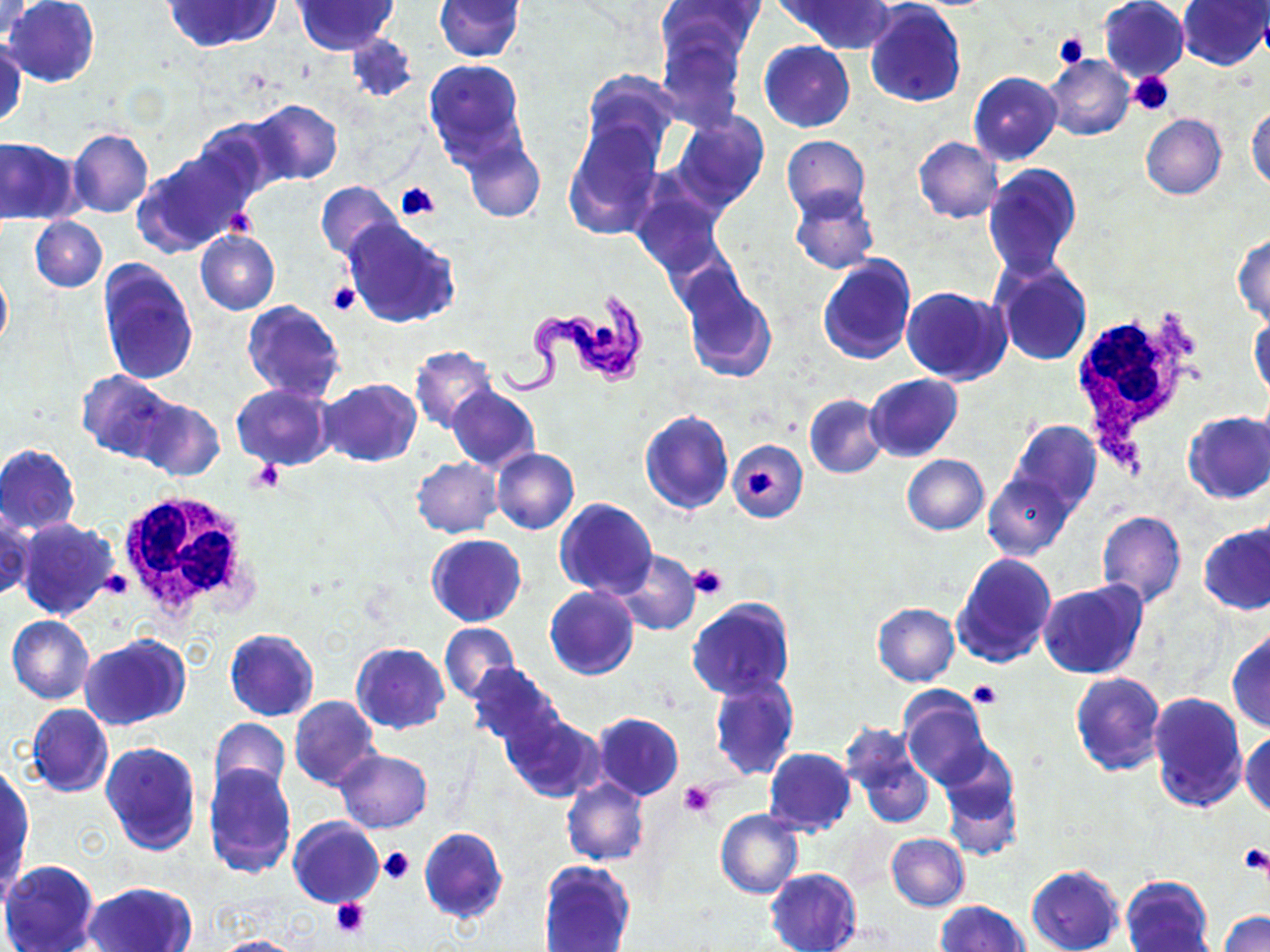

Summary:
  - Coordinate format: approximate bounding boxes as named x1/y1/x2/y2 corners in pixels
  - White blood cell locations: (x1=1066, y1=296, x2=1197, y2=477), (x1=115, y1=489, x2=262, y2=627)
  - Platelet locations: (x1=1051, y1=31, x2=1089, y2=69), (x1=1129, y1=71, x2=1176, y2=115), (x1=395, y1=183, x2=440, y2=222), (x1=224, y1=209, x2=258, y2=240), (x1=327, y1=281, x2=361, y2=317), (x1=248, y1=460, x2=286, y2=494), (x1=746, y1=469, x2=779, y2=497), (x1=689, y1=563, x2=729, y2=599), (x1=102, y1=567, x2=132, y2=598), (x1=968, y1=680, x2=1002, y2=707), (x1=679, y1=781, x2=717, y2=818), (x1=1240, y1=842, x2=1270, y2=877), (x1=379, y1=847, x2=414, y2=885), (x1=331, y1=897, x2=371, y2=939)
  - Uninfected red blood cell locations: (x1=0, y1=0, x2=35, y2=41), (x1=5, y1=0, x2=98, y2=87), (x1=165, y1=0, x2=278, y2=51), (x1=433, y1=0, x2=523, y2=60), (x1=789, y1=0, x2=896, y2=52), (x1=1098, y1=0, x2=1190, y2=82), (x1=1178, y1=0, x2=1269, y2=70), (x1=293, y1=1, x2=398, y2=54), (x1=656, y1=1, x2=758, y2=72), (x1=864, y1=1, x2=966, y2=107), (x1=345, y1=33, x2=417, y2=101), (x1=656, y1=36, x2=746, y2=133), (x1=1, y1=39, x2=25, y2=131), (x1=760, y1=41, x2=854, y2=131), (x1=1044, y1=56, x2=1135, y2=141), (x1=424, y1=58, x2=530, y2=172), (x1=580, y1=69, x2=681, y2=168), (x1=968, y1=71, x2=1062, y2=166), (x1=245, y1=99, x2=343, y2=187), (x1=1247, y1=107, x2=1270, y2=191), (x1=668, y1=111, x2=769, y2=211), (x1=1140, y1=114, x2=1227, y2=199), (x1=191, y1=119, x2=283, y2=206), (x1=562, y1=120, x2=664, y2=239), (x1=68, y1=128, x2=153, y2=218), (x1=781, y1=134, x2=870, y2=221), (x1=0, y1=137, x2=80, y2=225), (x1=462, y1=137, x2=545, y2=223), (x1=913, y1=137, x2=1003, y2=223), (x1=134, y1=149, x2=250, y2=257), (x1=984, y1=164, x2=1082, y2=279), (x1=628, y1=178, x2=727, y2=278), (x1=315, y1=181, x2=402, y2=262), (x1=789, y1=187, x2=879, y2=275), (x1=30, y1=216, x2=106, y2=292), (x1=342, y1=219, x2=461, y2=328), (x1=195, y1=230, x2=280, y2=315), (x1=1233, y1=233, x2=1270, y2=325), (x1=817, y1=254, x2=917, y2=365), (x1=992, y1=259, x2=1092, y2=365), (x1=97, y1=260, x2=199, y2=385), (x1=0, y1=266, x2=11, y2=353), (x1=680, y1=277, x2=778, y2=384), (x1=902, y1=287, x2=1010, y2=385), (x1=242, y1=300, x2=346, y2=402), (x1=1250, y1=312, x2=1269, y2=401), (x1=409, y1=345, x2=499, y2=434), (x1=77, y1=371, x2=177, y2=461), (x1=866, y1=374, x2=963, y2=462), (x1=319, y1=378, x2=421, y2=466), (x1=233, y1=384, x2=334, y2=470), (x1=447, y1=385, x2=539, y2=473), (x1=804, y1=394, x2=887, y2=479), (x1=135, y1=396, x2=223, y2=481), (x1=639, y1=411, x2=733, y2=515), (x1=1183, y1=411, x2=1270, y2=503), (x1=1007, y1=419, x2=1101, y2=515), (x1=727, y1=439, x2=808, y2=525), (x1=0, y1=444, x2=81, y2=534), (x1=492, y1=447, x2=579, y2=534), (x1=902, y1=454, x2=989, y2=534), (x1=411, y1=457, x2=502, y2=537), (x1=983, y1=473, x2=1076, y2=558), (x1=554, y1=499, x2=658, y2=600), (x1=1, y1=510, x2=33, y2=602), (x1=1095, y1=510, x2=1186, y2=608), (x1=14, y1=518, x2=120, y2=621), (x1=1200, y1=522, x2=1269, y2=614), (x1=426, y1=535, x2=525, y2=627), (x1=611, y1=550, x2=700, y2=636), (x1=952, y1=552, x2=1057, y2=669), (x1=1037, y1=581, x2=1146, y2=680), (x1=544, y1=586, x2=637, y2=680), (x1=686, y1=598, x2=795, y2=698), (x1=871, y1=603, x2=960, y2=686), (x1=7, y1=615, x2=95, y2=703), (x1=440, y1=623, x2=518, y2=704), (x1=225, y1=629, x2=319, y2=721), (x1=1227, y1=629, x2=1270, y2=732), (x1=81, y1=635, x2=189, y2=730), (x1=351, y1=642, x2=450, y2=734), (x1=465, y1=662, x2=565, y2=751), (x1=1070, y1=671, x2=1166, y2=775), (x1=709, y1=675, x2=799, y2=782), (x1=899, y1=686, x2=993, y2=790), (x1=1147, y1=691, x2=1248, y2=812), (x1=289, y1=694, x2=380, y2=790), (x1=27, y1=704, x2=113, y2=797), (x1=593, y1=713, x2=684, y2=800), (x1=503, y1=714, x2=604, y2=802), (x1=209, y1=718, x2=292, y2=803), (x1=843, y1=727, x2=935, y2=830), (x1=1241, y1=728, x2=1270, y2=818), (x1=100, y1=741, x2=202, y2=854), (x1=938, y1=744, x2=1023, y2=860), (x1=763, y1=748, x2=857, y2=836), (x1=336, y1=749, x2=432, y2=833), (x1=202, y1=763, x2=297, y2=879), (x1=1, y1=766, x2=32, y2=875), (x1=562, y1=778, x2=649, y2=866), (x1=716, y1=808, x2=803, y2=898), (x1=288, y1=817, x2=384, y2=907), (x1=419, y1=827, x2=508, y2=925), (x1=886, y1=832, x2=969, y2=912), (x1=1, y1=859, x2=99, y2=952), (x1=539, y1=859, x2=635, y2=952), (x1=1026, y1=865, x2=1124, y2=952), (x1=765, y1=869, x2=861, y2=952), (x1=1121, y1=875, x2=1214, y2=952), (x1=84, y1=881, x2=196, y2=952), (x1=934, y1=900, x2=1030, y2=952), (x1=1220, y1=911, x2=1270, y2=952), (x1=210, y1=935, x2=310, y2=952)
  - Trypanosoma brucei locations: (x1=495, y1=288, x2=651, y2=398)
  - Slide-level diagnosis: Trypanosoma brucei
  - Preparation: thin blood smear
  - Stain: May-Grünwald-Giemsa
  - Modality: optical microscopy
  - Field of view: one of a larger specimen
  - Image size: 1270×952 pixels
  - Magnification: 1000x